Outline each Plasmodium vivax-infected red blood cell.
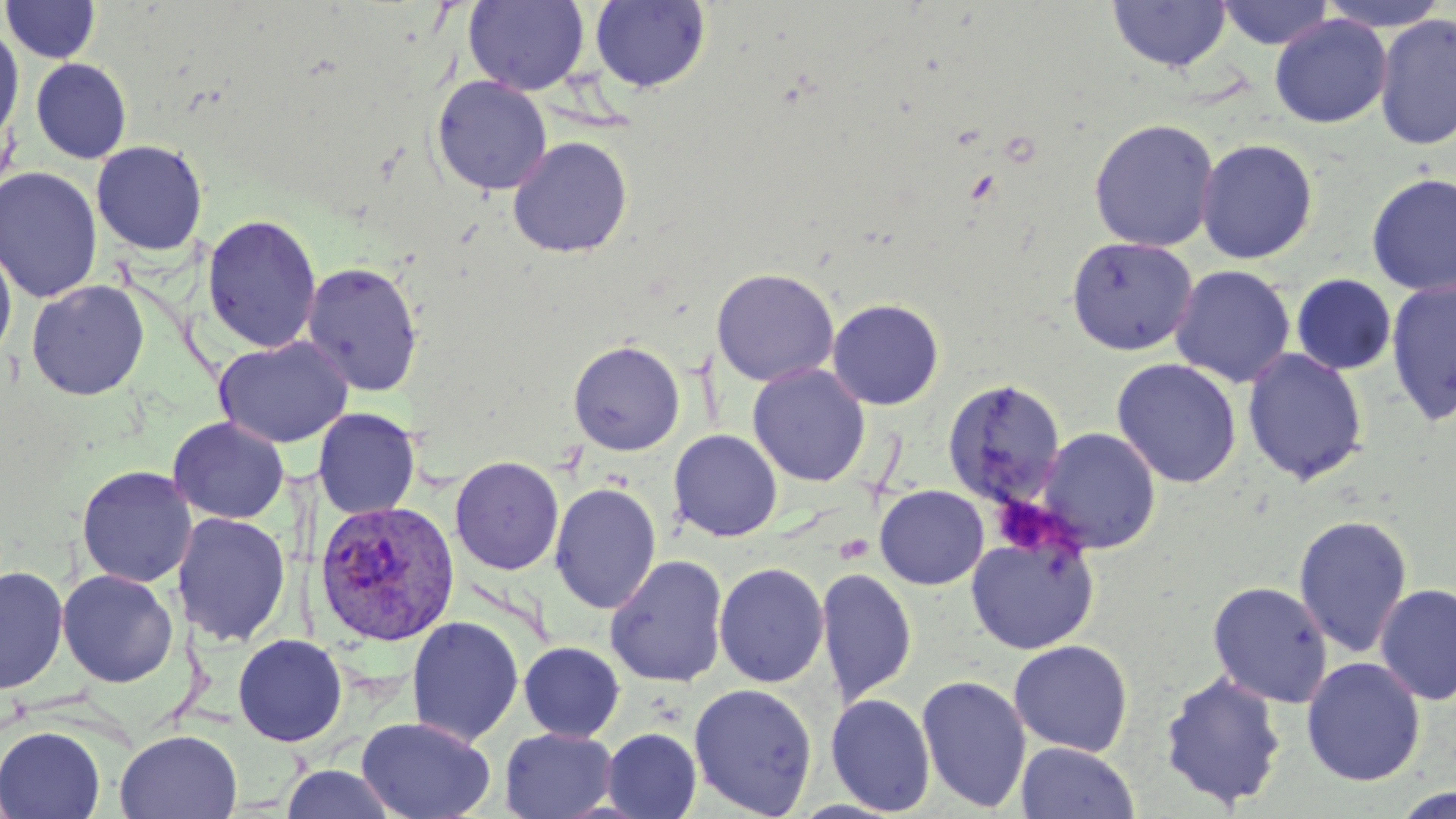

Approximate bounding boxes as (x1, y1, x2, y2) in pixels.
Plasmodium vivax-infected red blood cells: (314, 500, 460, 646).

Platelet locations: (990, 494, 1070, 557). Uninfected red blood cell locations: (2, 0, 101, 63), (1107, 0, 1232, 73), (1217, 0, 1335, 50), (1317, 0, 1453, 31), (463, 1, 589, 96), (589, 1, 711, 93), (1374, 13, 1456, 151), (1269, 14, 1392, 128), (0, 22, 24, 150), (31, 58, 132, 164), (430, 76, 552, 195), (1088, 118, 1219, 252), (507, 135, 634, 258), (1195, 137, 1318, 264), (91, 140, 208, 256), (0, 166, 103, 302), (1366, 171, 1456, 296), (202, 214, 322, 354), (1066, 236, 1198, 356), (0, 241, 17, 365), (301, 261, 424, 397), (1170, 264, 1296, 387), (711, 267, 839, 388), (1291, 273, 1397, 376), (1385, 279, 1456, 426), (26, 280, 150, 401), (827, 299, 945, 410), (213, 336, 354, 448), (568, 340, 685, 456), (1242, 347, 1369, 485), (1111, 357, 1242, 489), (747, 363, 870, 487), (942, 377, 1066, 509), (313, 407, 420, 520), (168, 417, 290, 524), (1036, 426, 1162, 553), (668, 429, 783, 542), (449, 455, 564, 575), (76, 465, 197, 588), (550, 482, 661, 613), (875, 485, 989, 590), (174, 511, 291, 646), (1293, 514, 1413, 658), (965, 531, 1100, 654), (605, 554, 729, 687), (714, 562, 829, 688), (0, 566, 69, 695), (816, 567, 917, 707), (57, 569, 179, 687), (1207, 581, 1332, 708), (1375, 582, 1456, 705), (406, 615, 524, 747), (232, 634, 348, 747), (1008, 639, 1133, 756), (518, 641, 625, 742), (1301, 656, 1425, 786), (1160, 671, 1287, 809), (916, 673, 1032, 813), (688, 682, 818, 818), (826, 693, 935, 816), (356, 716, 495, 818), (0, 726, 106, 819), (499, 727, 618, 818), (601, 728, 701, 818), (114, 729, 243, 819), (1016, 741, 1139, 819), (279, 764, 399, 819), (1392, 784, 1455, 817). Slide-level diagnosis: Plasmodium vivax. Image is 1456×819 pixels. May-Grünwald-Giemsa stain. One field of a larger specimen. Thin blood smear. Optical microscopy. 1000x magnification.